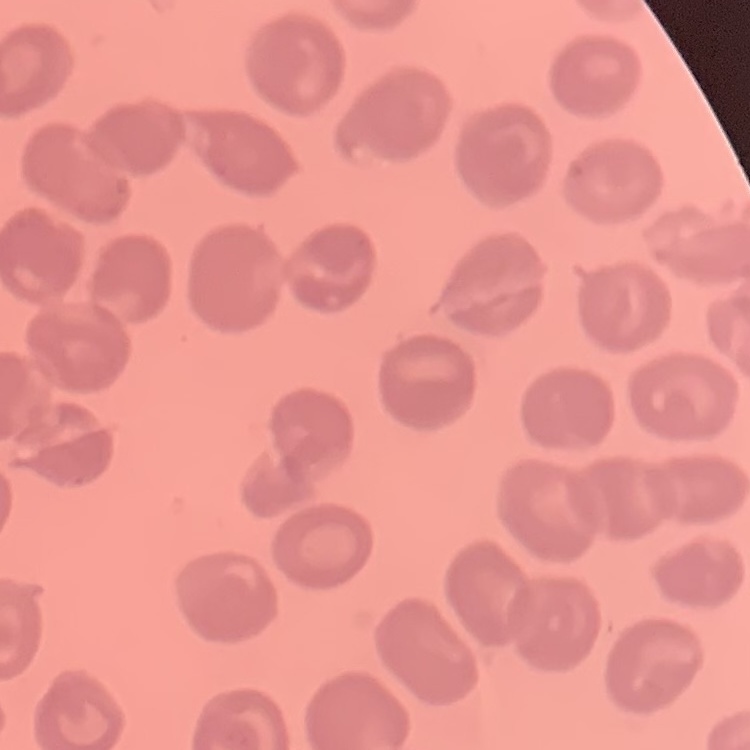
Summary:
  - Erythrocyte morphology: no rouleaux formation
  - Image type: one tile cut from a larger photomicrograph
  - Stain: Field's or Giemsa
  - Preparation: thin blood smear